Assess the morphology of the red blood cells.
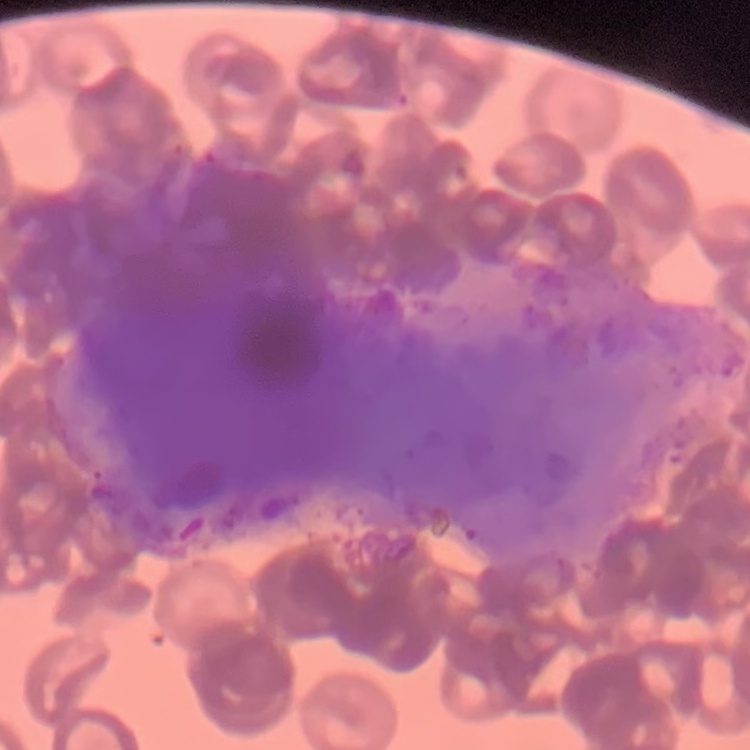

They show rouleaux formation.

Square crop of a larger photomicrograph. Field's or Giemsa stain. Thin blood smear.